Assess this cell for malaria.
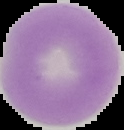
It is uninfected.

image type = segmented cell region on a black background
image size = 124×130 pixels
preparation = thin blood film